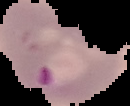

image_type: segmented cell region on a black background
preparation: thin blood smear
image_size: 130×106 pixels
result: malaria parasites detected